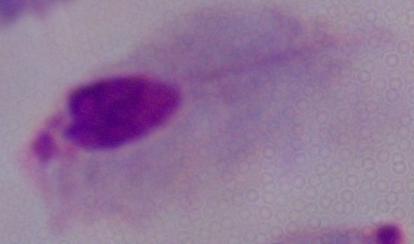
Summary:
  - Identification: trichomonad
  - Modality: micrograph
  - Magnification: 1000x